Assess this cell for malaria.
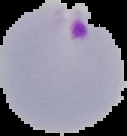

It is parasitized.

From a thin blood film. Image is 127×136 pixels. Cell region segmented out of the field of view; the surrounding area is masked to black.